Describe the morphology of the erythrocytes.
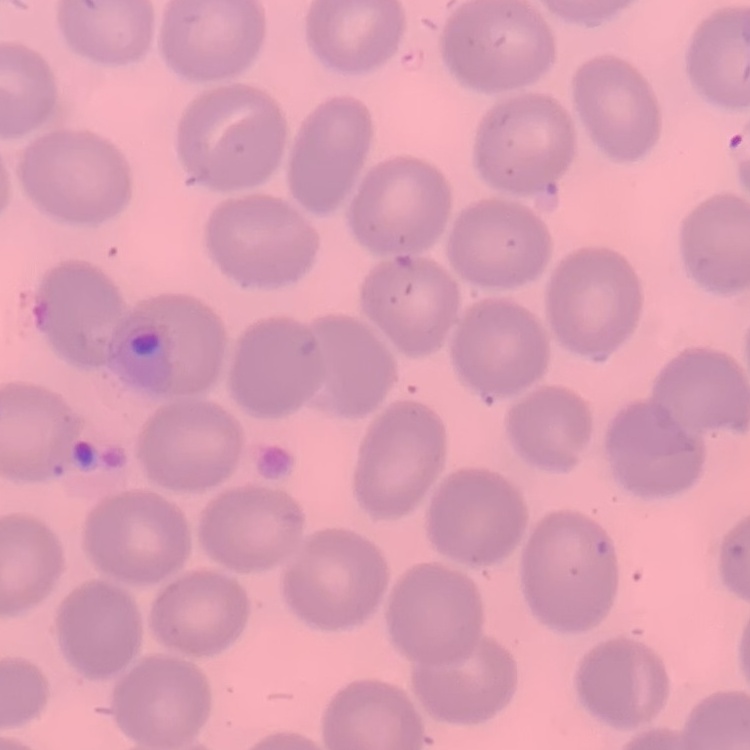

They show no rouleaux formation.

One tile cut from a larger photomicrograph. Thin blood smear. Stained with either Field's or Giemsa.